Identify the parasite.
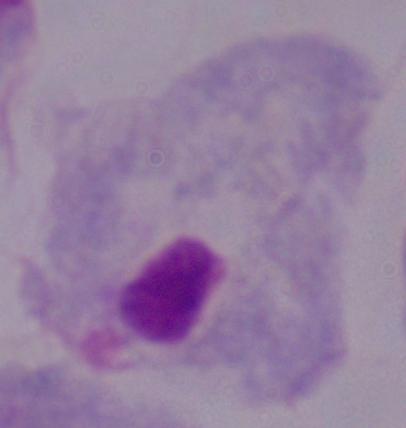

A trichomonad.

Photomicrograph. 1000x magnification.